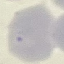
Summary:
  - Result: no malaria parasites detected
  - Preparation: thin blood film
  - Image type: automatically extracted cell patch, resized to 64 × 64 pixels
  - Stain: Giemsa
  - Capture: smartphone through the microscope eyepiece